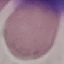
result: no malaria parasites seen
preparation: thin smear
stain: Giemsa
capture: smartphone camera at the microscope eyepiece
image_type: cell patch, automatically extracted from a larger field of view and resized to 64 × 64 pixels